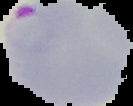
Image is 133×106 pixels. The area outside the segmented cell region is set to black. From a thin blood smear. Malaria status: parasitized.